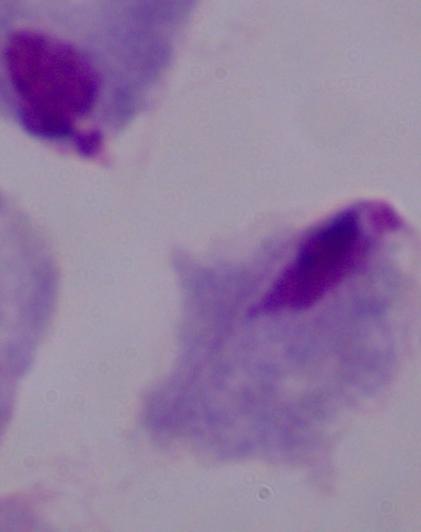

modality: photomicrograph
identification: trichomonad
magnification: 1000x